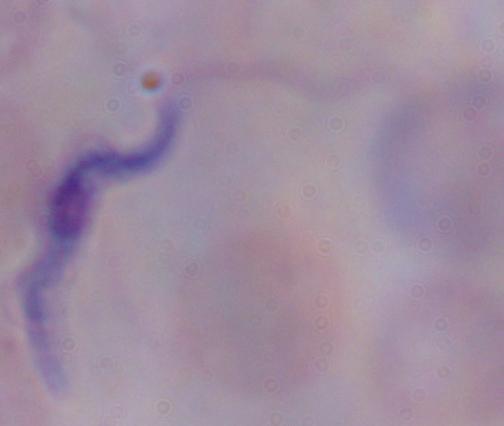 Photomicrograph. A trypanosome is seen. Captured at 1000x magnification.